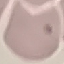
Summary:
  - Result: negative for malaria parasites
  - Stain: Giemsa
  - Preparation: thin smear
  - Image type: cell patch, automatically extracted from a larger field of view and resized to 64 × 64 pixels
  - Capture: smartphone camera at the microscope eyepiece